Locate and identify every blood parasite.
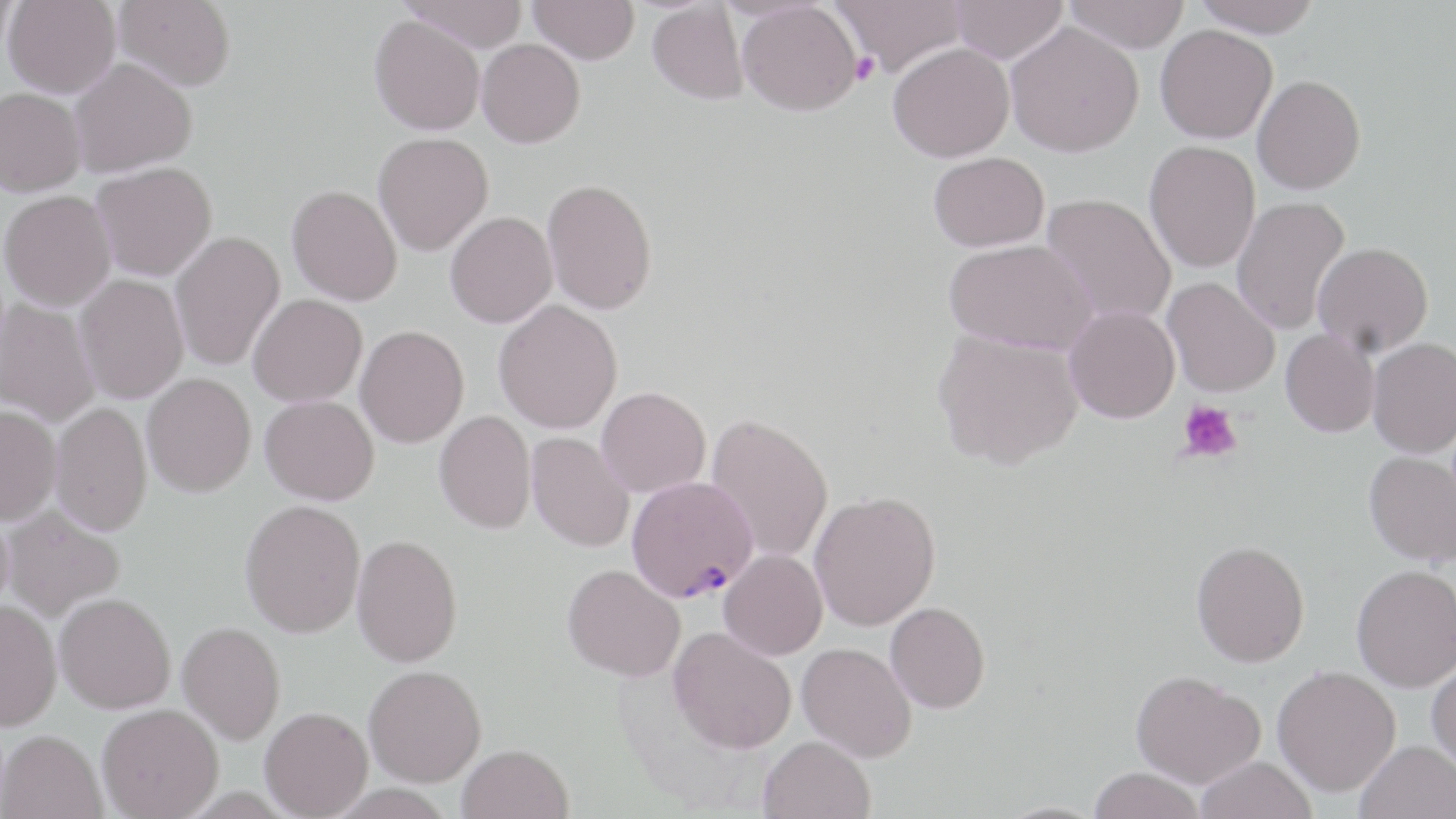
Approximate bounding boxes as named x1/y1/x2/y2 corners in pixels.
Plasmodium falciparum-infected red blood cells: (x1=626, y1=476, x2=758, y2=603).
No Plasmodium ovale, Plasmodium malariae, Plasmodium vivax, Babesia divergens, or Trypanosoma brucei observed.

Platelet locations: (x1=848, y1=51, x2=881, y2=85), (x1=1178, y1=400, x2=1243, y2=465). Uninfected red blood cell locations: (x1=0, y1=0, x2=17, y2=58), (x1=3, y1=0, x2=121, y2=98), (x1=113, y1=0, x2=236, y2=91), (x1=401, y1=0, x2=529, y2=53), (x1=529, y1=0, x2=640, y2=64), (x1=832, y1=0, x2=967, y2=78), (x1=950, y1=0, x2=1067, y2=64), (x1=1064, y1=0, x2=1190, y2=52), (x1=1191, y1=0, x2=1322, y2=37), (x1=647, y1=2, x2=748, y2=104), (x1=737, y1=2, x2=862, y2=115), (x1=369, y1=15, x2=485, y2=135), (x1=1005, y1=22, x2=1143, y2=157), (x1=1155, y1=24, x2=1277, y2=143), (x1=476, y1=38, x2=585, y2=147), (x1=888, y1=42, x2=1014, y2=163), (x1=68, y1=58, x2=197, y2=176), (x1=1252, y1=74, x2=1366, y2=194), (x1=0, y1=88, x2=85, y2=197), (x1=373, y1=132, x2=493, y2=256), (x1=1144, y1=140, x2=1261, y2=273), (x1=928, y1=151, x2=1050, y2=252), (x1=91, y1=162, x2=216, y2=281), (x1=542, y1=178, x2=658, y2=315), (x1=287, y1=185, x2=402, y2=305), (x1=0, y1=191, x2=115, y2=311), (x1=1041, y1=193, x2=1177, y2=327), (x1=1231, y1=196, x2=1350, y2=335), (x1=445, y1=211, x2=557, y2=328), (x1=170, y1=230, x2=285, y2=371), (x1=944, y1=238, x2=1096, y2=354), (x1=1312, y1=242, x2=1434, y2=356), (x1=75, y1=274, x2=189, y2=404), (x1=1163, y1=277, x2=1280, y2=397), (x1=248, y1=293, x2=367, y2=407), (x1=1, y1=298, x2=100, y2=428), (x1=493, y1=300, x2=623, y2=434), (x1=1064, y1=305, x2=1180, y2=423), (x1=355, y1=325, x2=469, y2=448), (x1=1280, y1=328, x2=1380, y2=437), (x1=932, y1=329, x2=1084, y2=470), (x1=1368, y1=337, x2=1456, y2=457), (x1=142, y1=373, x2=256, y2=497), (x1=596, y1=386, x2=712, y2=497), (x1=260, y1=395, x2=379, y2=505), (x1=50, y1=401, x2=152, y2=536), (x1=0, y1=405, x2=61, y2=525), (x1=434, y1=409, x2=537, y2=534), (x1=706, y1=413, x2=834, y2=563), (x1=527, y1=431, x2=635, y2=552), (x1=1364, y1=451, x2=1456, y2=566), (x1=808, y1=491, x2=941, y2=631), (x1=240, y1=499, x2=365, y2=637), (x1=3, y1=506, x2=125, y2=621), (x1=352, y1=533, x2=463, y2=667), (x1=1191, y1=540, x2=1310, y2=666), (x1=719, y1=549, x2=828, y2=660), (x1=563, y1=564, x2=686, y2=682), (x1=1352, y1=564, x2=1456, y2=691), (x1=55, y1=592, x2=176, y2=713), (x1=0, y1=600, x2=61, y2=730), (x1=885, y1=602, x2=991, y2=713), (x1=177, y1=621, x2=286, y2=744), (x1=669, y1=626, x2=796, y2=753), (x1=797, y1=642, x2=917, y2=762), (x1=1427, y1=659, x2=1456, y2=771), (x1=364, y1=664, x2=487, y2=786), (x1=1272, y1=665, x2=1400, y2=796), (x1=1131, y1=669, x2=1265, y2=788), (x1=96, y1=704, x2=223, y2=819), (x1=260, y1=706, x2=373, y2=818), (x1=1, y1=728, x2=106, y2=819), (x1=759, y1=735, x2=876, y2=819), (x1=1355, y1=741, x2=1456, y2=819), (x1=458, y1=743, x2=574, y2=819), (x1=1196, y1=756, x2=1317, y2=819), (x1=1088, y1=767, x2=1206, y2=819). Slide-level diagnosis: Plasmodium falciparum. Image is 1456×819 pixels. One field of a larger specimen. Thin blood smear. Captured at 1000x magnification. Light microscopy. May-Grünwald-Giemsa-stained preparation.